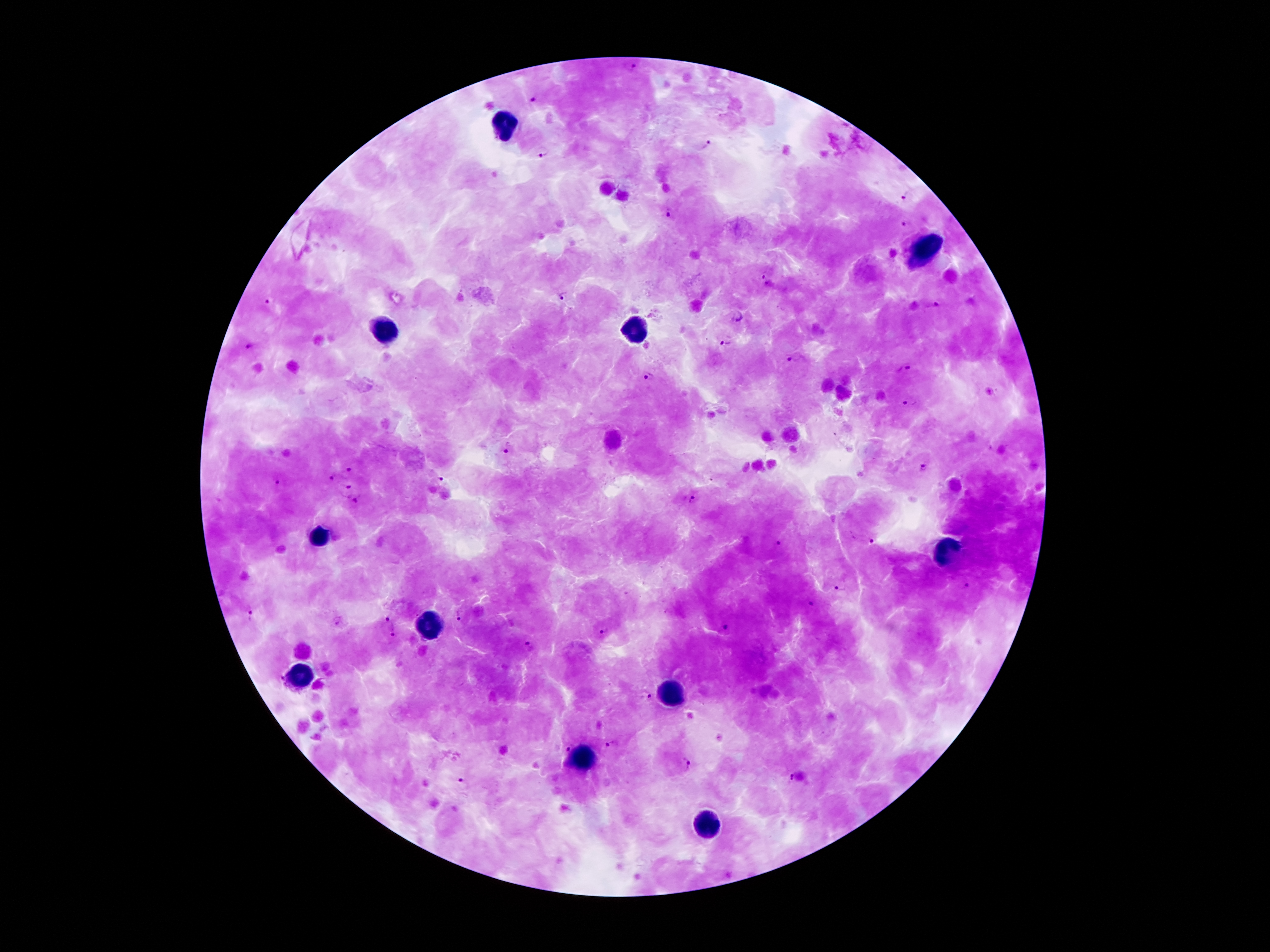
Approximate centers as {x, y} in pixels.
Summary:
  - Malaria parasite locations: {627, 65}, {533, 99}, {706, 146}, {543, 151}, {907, 194}, {669, 214}, {907, 225}, {766, 280}, {567, 296}, {269, 301}, {934, 306}, {737, 319}, {725, 344}, {249, 346}, {795, 358}, {903, 369}, {648, 376}, {910, 399}, {505, 450}, {923, 467}, {348, 470}, {331, 478}, {279, 481}, {437, 482}, {345, 488}, {694, 496}, {354, 501}, {870, 541}, {780, 545}, {842, 584}, {966, 585}, {809, 601}, {250, 614}, {459, 615}, {386, 619}, {336, 620}, {724, 629}, {601, 631}, {392, 635}, {531, 645}, {644, 693}, {611, 742}, {567, 748}, {688, 762}, {790, 779}, {463, 786}
  - Leukocyte locations: {507, 124}, {920, 250}, {629, 331}, {384, 333}, {320, 536}, {950, 551}, {426, 627}, {295, 674}, {676, 694}, {579, 761}, {708, 826}
  - Image size: 1270×952 pixels
  - Preparation: thick blood smear
  - Magnification: 100x
  - Stain: Giemsa
  - Capture: smartphone through the microscope eyepiece
  - Patient malaria status: positive for Plasmodium falciparum
  - Field of view: single